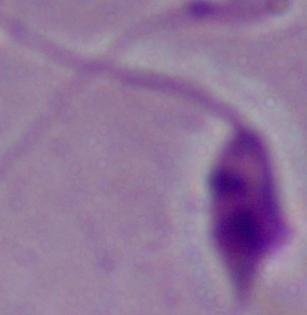

magnification: 1000x
modality: photomicrograph
identification: Leishmania